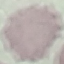
Summary:
  - Result: negative for malaria parasites
  - Preparation: thin blood film
  - Image type: cell patch, automatically extracted from a larger field of view and resized to 64 × 64 pixels
  - Stain: Giemsa
  - Capture: smartphone camera at the microscope eyepiece